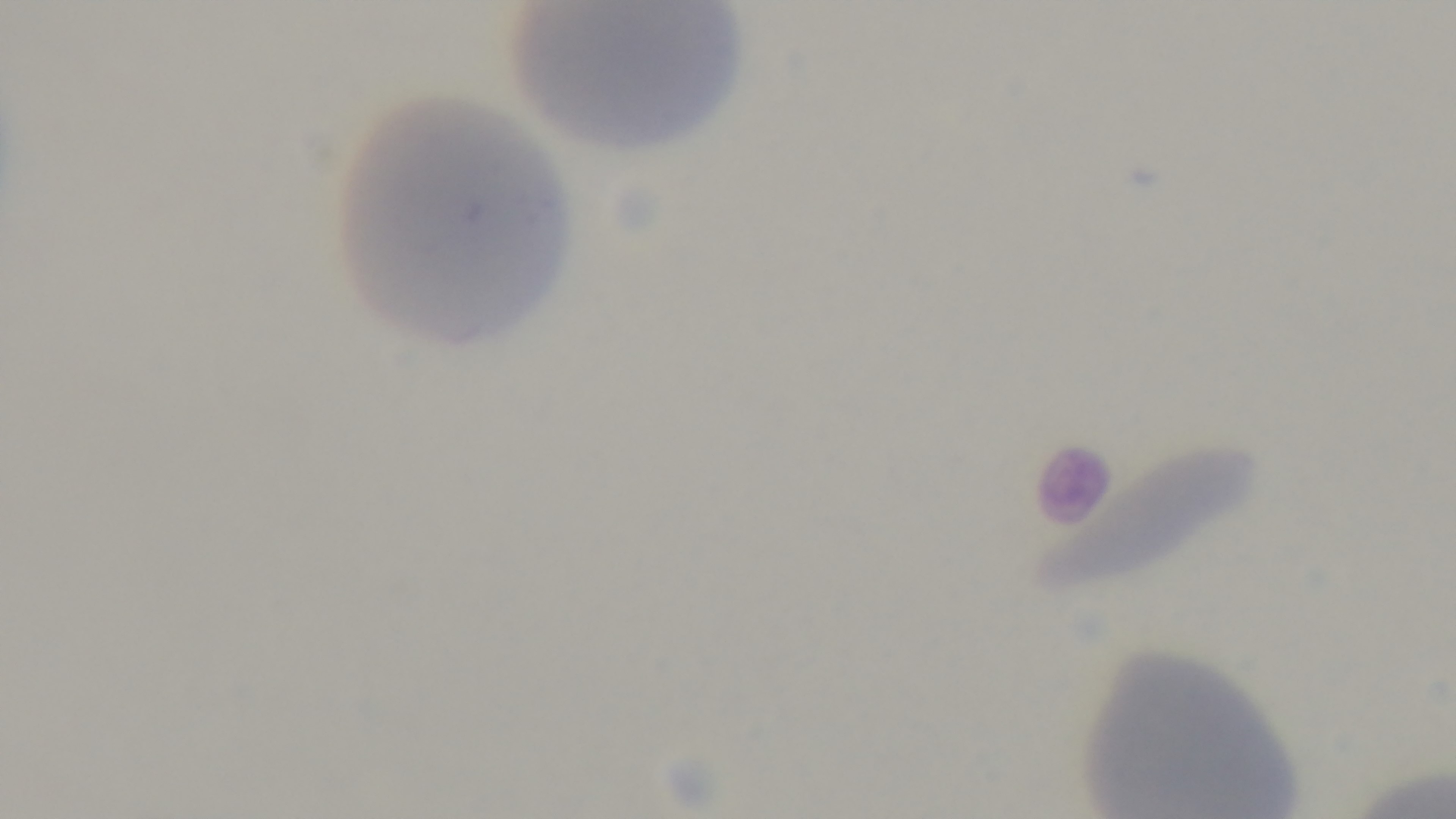
Giemsa-stained. Preparation: thin. Malaria status: negative. One field from the slide. 100x oil-immersion objective. Photomicrograph. Mounted 4K digital camera.